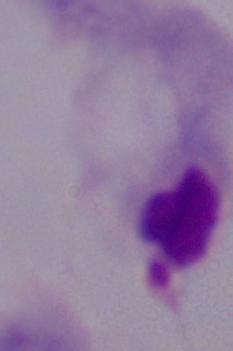
A trichomonad is shown. Micrograph. 1000x magnification.